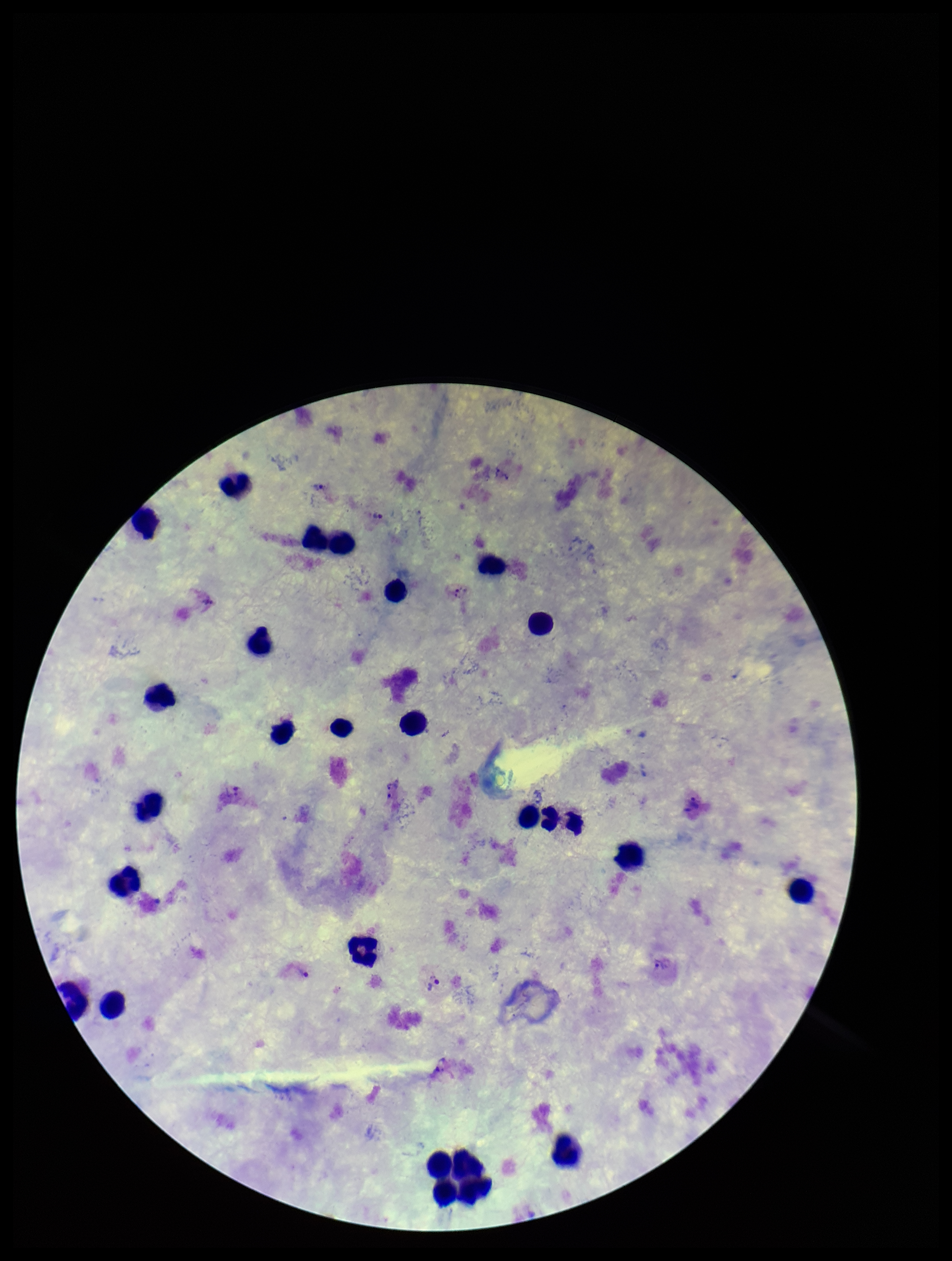
stain = Giemsa
patient malaria status = positive
image size = 952×1261 pixels
capture = smartphone photograph through the microscope eyepiece
species reported for this patient = Plasmodium vivax
parasite count = 7
Plasmodium parasites = seen
leukocyte count = 25
field of view = single
preparation = thick smear